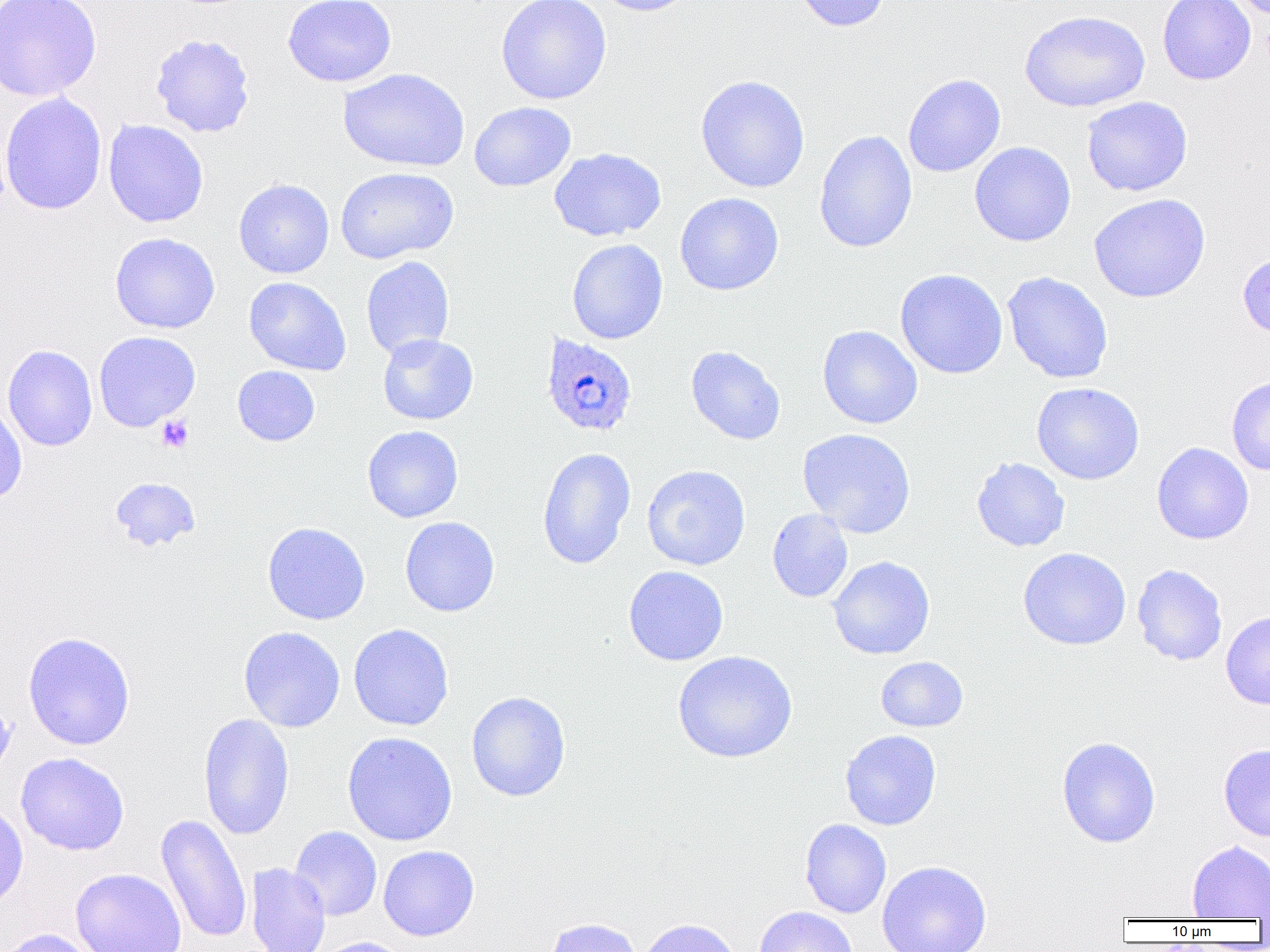

Summary:
  - Coordinate format: approximate bounding boxes as named x1/y1/x2/y2 corners in pixels
  - Plasmodium ovale-infected red blood cell locations: (x1=540, y1=333, x2=637, y2=437)
  - Uninfected red blood cell locations: (x1=0, y1=0, x2=102, y2=101), (x1=282, y1=0, x2=396, y2=87), (x1=496, y1=0, x2=612, y2=105), (x1=590, y1=0, x2=698, y2=16), (x1=791, y1=0, x2=892, y2=32), (x1=1157, y1=0, x2=1256, y2=85), (x1=1020, y1=10, x2=1150, y2=113), (x1=150, y1=33, x2=255, y2=138), (x1=337, y1=67, x2=470, y2=172), (x1=903, y1=74, x2=1006, y2=178), (x1=695, y1=75, x2=810, y2=193), (x1=0, y1=92, x2=107, y2=215), (x1=1082, y1=96, x2=1193, y2=197), (x1=469, y1=101, x2=576, y2=192), (x1=103, y1=119, x2=209, y2=228), (x1=814, y1=130, x2=917, y2=254), (x1=970, y1=141, x2=1076, y2=247), (x1=549, y1=147, x2=666, y2=242), (x1=335, y1=167, x2=459, y2=263), (x1=233, y1=178, x2=334, y2=278), (x1=674, y1=192, x2=784, y2=296), (x1=1088, y1=193, x2=1210, y2=303), (x1=110, y1=232, x2=220, y2=334), (x1=567, y1=239, x2=668, y2=344), (x1=1238, y1=251, x2=1270, y2=339), (x1=361, y1=256, x2=454, y2=359), (x1=895, y1=268, x2=1008, y2=379), (x1=1002, y1=271, x2=1113, y2=384), (x1=244, y1=277, x2=352, y2=376), (x1=817, y1=325, x2=923, y2=429), (x1=93, y1=331, x2=200, y2=432), (x1=377, y1=333, x2=479, y2=425), (x1=2, y1=344, x2=98, y2=451), (x1=685, y1=345, x2=786, y2=445), (x1=232, y1=366, x2=320, y2=446), (x1=1226, y1=376, x2=1270, y2=476), (x1=1032, y1=382, x2=1144, y2=485), (x1=0, y1=400, x2=27, y2=506), (x1=362, y1=425, x2=463, y2=523), (x1=797, y1=428, x2=916, y2=538), (x1=1152, y1=442, x2=1254, y2=545), (x1=537, y1=447, x2=636, y2=569), (x1=971, y1=456, x2=1070, y2=552), (x1=642, y1=465, x2=751, y2=570), (x1=109, y1=476, x2=200, y2=552), (x1=767, y1=509, x2=853, y2=603), (x1=400, y1=517, x2=500, y2=617), (x1=263, y1=522, x2=370, y2=625), (x1=1018, y1=547, x2=1131, y2=650), (x1=827, y1=556, x2=935, y2=660), (x1=1132, y1=564, x2=1228, y2=665), (x1=623, y1=565, x2=729, y2=665), (x1=1220, y1=611, x2=1270, y2=710), (x1=348, y1=623, x2=453, y2=731), (x1=239, y1=626, x2=345, y2=732), (x1=22, y1=631, x2=136, y2=750), (x1=672, y1=650, x2=797, y2=763), (x1=876, y1=656, x2=968, y2=732), (x1=466, y1=691, x2=570, y2=802), (x1=0, y1=696, x2=15, y2=779), (x1=198, y1=712, x2=295, y2=841), (x1=840, y1=729, x2=942, y2=831), (x1=342, y1=732, x2=457, y2=846), (x1=1057, y1=736, x2=1161, y2=848), (x1=1219, y1=744, x2=1270, y2=842), (x1=15, y1=752, x2=129, y2=856), (x1=0, y1=802, x2=28, y2=913), (x1=155, y1=813, x2=252, y2=944), (x1=800, y1=819, x2=891, y2=918), (x1=289, y1=826, x2=382, y2=921), (x1=1187, y1=840, x2=1270, y2=920), (x1=378, y1=845, x2=479, y2=941), (x1=876, y1=860, x2=992, y2=952), (x1=246, y1=862, x2=330, y2=952), (x1=70, y1=868, x2=187, y2=952), (x1=753, y1=906, x2=858, y2=952), (x1=543, y1=917, x2=643, y2=952), (x1=635, y1=918, x2=743, y2=952), (x1=0, y1=928, x2=100, y2=952), (x1=312, y1=937, x2=412, y2=952)
  - Platelet locations: (x1=157, y1=415, x2=193, y2=453)
  - Slide-level diagnosis: Plasmodium ovale
  - Field of view: single
  - Magnification: 1000x
  - Modality: optical microscopy
  - Image size: 1270×952 pixels
  - Preparation: thin blood smear